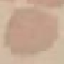

Summary:
  - Result: negative for malaria parasites
  - Stain: Giemsa
  - Image type: automatically extracted cell patch, resized to 64 × 64 pixels
  - Capture: smartphone camera at the microscope eyepiece
  - Preparation: thin blood smear